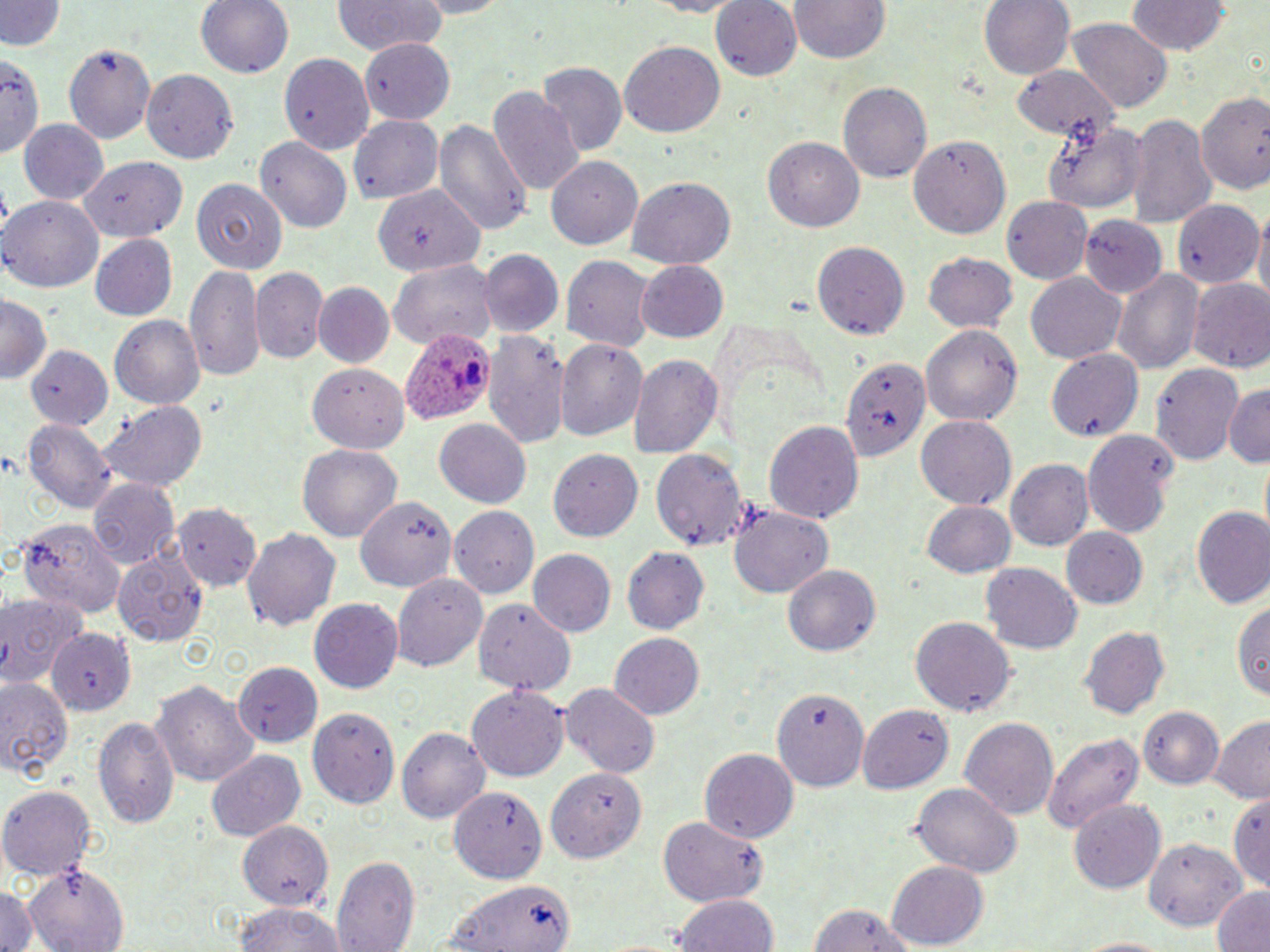
Approximate bounding boxes as [x1, y1, x2, y2] in pixels. Plasmodium ovale-infected red blood cell locations: [401, 328, 497, 428]. Uninfected red blood cell locations: [0, 0, 63, 53], [197, 0, 295, 78], [330, 0, 449, 57], [631, 0, 750, 17], [710, 0, 802, 80], [979, 0, 1073, 81], [792, 1, 890, 65], [1126, 2, 1230, 57], [1068, 21, 1172, 111], [359, 38, 456, 124], [621, 39, 726, 137], [63, 42, 157, 141], [0, 50, 42, 162], [278, 52, 376, 154], [537, 64, 626, 156], [1010, 64, 1119, 139], [142, 68, 239, 163], [837, 81, 932, 183], [488, 85, 584, 198], [1198, 86, 1270, 193], [1126, 112, 1216, 231], [351, 114, 445, 204], [433, 117, 531, 237], [19, 119, 109, 206], [1044, 119, 1147, 212], [909, 133, 1011, 239], [257, 137, 352, 233], [766, 137, 863, 232], [80, 155, 186, 242], [546, 157, 644, 246], [193, 178, 287, 275], [627, 178, 736, 268], [372, 188, 482, 277], [2, 195, 106, 292], [1003, 196, 1092, 285], [1171, 199, 1263, 288], [1252, 211, 1270, 311], [1080, 216, 1166, 297], [88, 233, 178, 321], [811, 241, 910, 340], [479, 250, 563, 337], [562, 252, 656, 347], [925, 252, 1017, 335], [386, 257, 497, 351], [635, 262, 728, 341], [186, 265, 265, 380], [252, 268, 328, 364], [1116, 271, 1204, 375], [1025, 272, 1127, 363], [1188, 280, 1270, 375], [313, 284, 395, 369], [0, 294, 51, 386], [110, 314, 207, 410], [922, 323, 1023, 426], [484, 329, 567, 452], [24, 338, 120, 434], [556, 339, 648, 444], [23, 345, 115, 432], [1044, 349, 1145, 437], [628, 353, 723, 461], [845, 355, 929, 465], [302, 358, 407, 454], [1152, 360, 1245, 464], [1223, 384, 1270, 467], [98, 400, 210, 492], [916, 417, 1015, 509], [24, 418, 117, 513], [433, 418, 530, 507], [764, 419, 864, 524], [1082, 429, 1182, 538], [296, 444, 402, 542], [652, 447, 750, 553], [552, 449, 643, 542], [1005, 459, 1093, 551], [88, 474, 179, 571], [355, 493, 461, 596], [922, 500, 1014, 578], [442, 503, 541, 602], [173, 505, 262, 592], [1190, 507, 1270, 609], [729, 508, 831, 597], [17, 515, 128, 619], [245, 526, 341, 634], [1059, 526, 1149, 610], [621, 548, 708, 636], [113, 549, 213, 645], [527, 549, 614, 639], [982, 563, 1083, 654], [783, 565, 880, 660], [392, 572, 488, 673], [0, 589, 88, 687], [1232, 593, 1269, 700], [309, 599, 403, 694], [473, 600, 575, 694], [912, 616, 1015, 717], [1081, 626, 1170, 721], [46, 629, 135, 716], [610, 633, 704, 721], [237, 662, 323, 748], [0, 678, 73, 771], [151, 680, 259, 787], [561, 682, 661, 776], [467, 686, 568, 782], [772, 686, 869, 793], [1137, 705, 1225, 790], [308, 706, 402, 806], [857, 706, 952, 793], [95, 713, 181, 832], [960, 715, 1059, 820], [1209, 715, 1270, 801], [399, 726, 490, 826], [1044, 729, 1143, 838], [700, 747, 800, 842], [205, 748, 306, 841], [544, 765, 644, 866], [1, 784, 96, 880], [911, 785, 1022, 878], [451, 788, 547, 883], [1230, 789, 1270, 889], [1070, 799, 1165, 895], [659, 818, 770, 905], [235, 823, 334, 908], [1145, 841, 1246, 927], [333, 854, 418, 952], [886, 863, 989, 946], [25, 866, 127, 951], [437, 879, 575, 950], [0, 887, 43, 952], [1209, 887, 1270, 952], [673, 893, 778, 952], [807, 900, 920, 952], [232, 903, 349, 952], [1061, 934, 1185, 951]. Slide-level diagnosis: Plasmodium ovale. Image is 1270×952 pixels. Optical microscopy. May-Grünwald-Giemsa-stained preparation. One field of a larger specimen. 1000x magnification. Thin blood film.